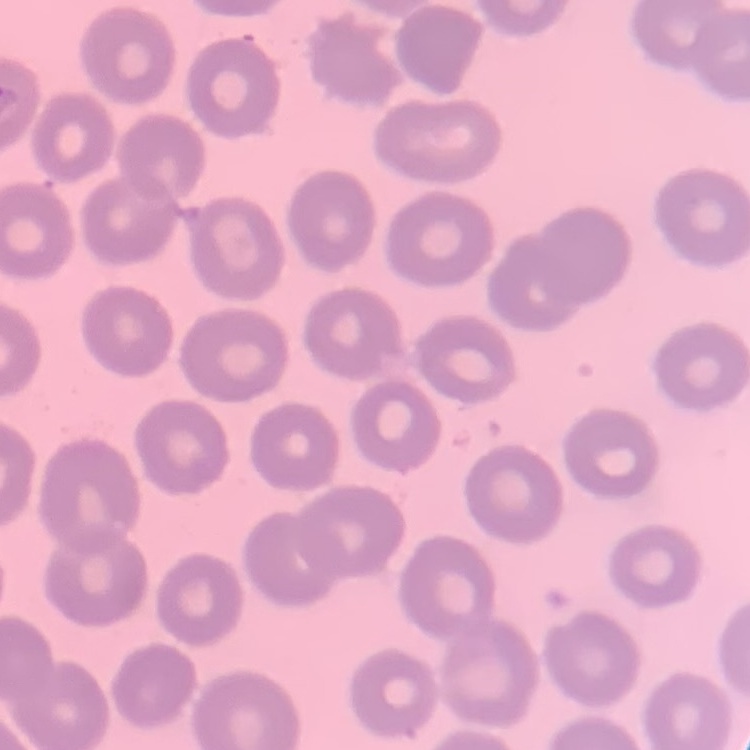
red_blood_cell_morphology: no rouleaux formation
stain: Field's or Giemsa
preparation: thin blood film
image_type: square crop of a larger photomicrograph